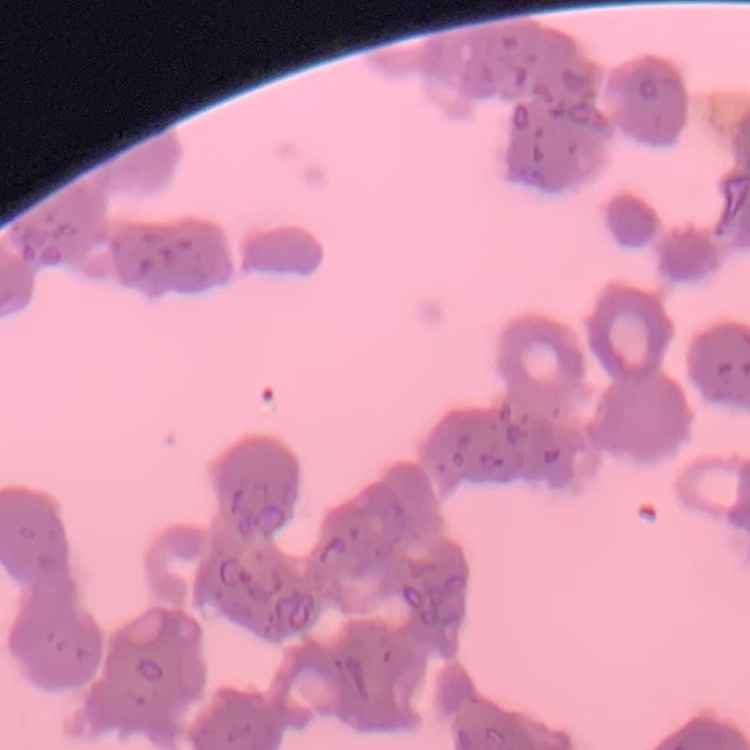

The red blood cells exhibit rouleaux formation. Stained with either Field's or Giemsa. Thin blood film. One tile cut from a larger photomicrograph.